Assess this cell for malaria.
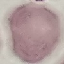
Uninfected.

Giemsa stain. Thin blood smear. Photographed with a smartphone camera at the microscope eyepiece. Automatically extracted cell patch, resized to 64 × 64 pixels.